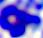
A leukocyte is seen. Photomicrograph. 400x magnification.